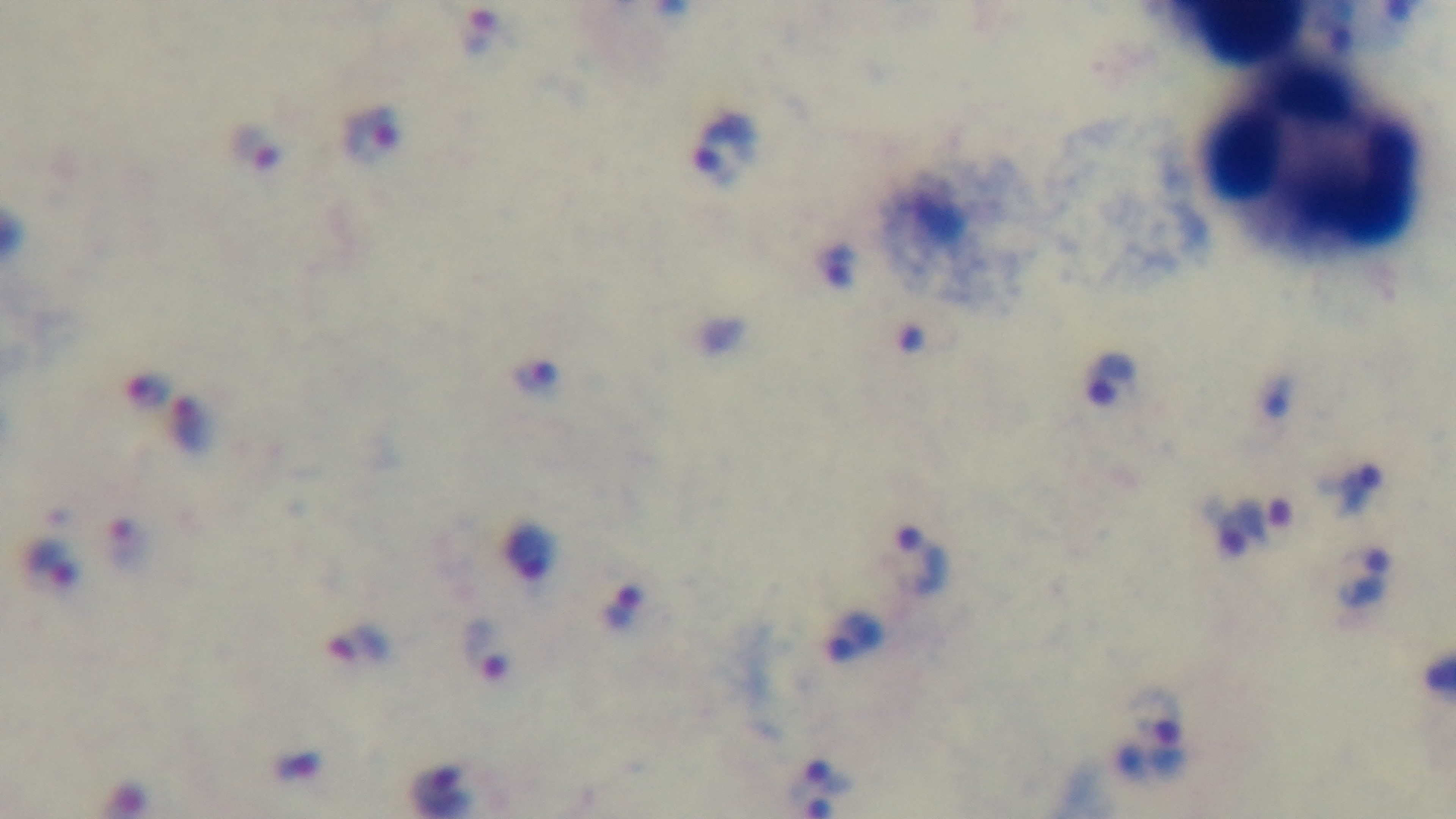

Summary:
  - Field of view: single
  - Stain: Giemsa
  - Objective: 100x oil immersion
  - Preparation: thick smear
  - Modality: light microscopy
  - Capture: mounted 4K digital camera
  - Malaria status: positive